Mark where leukocytes are.
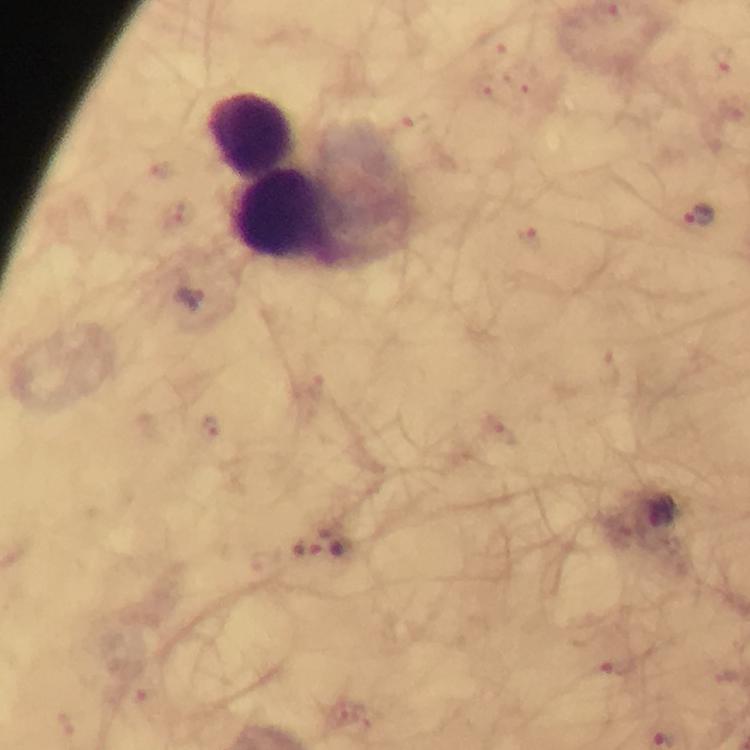

Approximate centers as {x, y} in pixels.
Leukocytes: {252, 134}, {286, 218}.

Malaria parasite locations: {492, 44}, {722, 60}, {526, 84}, {487, 86}, {732, 107}, {411, 127}, {158, 169}, {178, 215}, {702, 219}, {532, 236}, {188, 298}, {210, 427}, {504, 433}, {335, 542}, {306, 549}, {619, 670}, {146, 700}, {65, 722}. Thick blood film. From a malaria diagnostic workup. Photographed through the microscope with a smartphone camera. Image is 750×750 pixels. Cropped region of a single field of view. Giemsa stain. Immersion oil was used. 100x magnification.